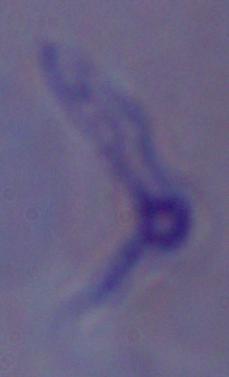

modality = micrograph
identification = trypanosome
magnification = 1000x